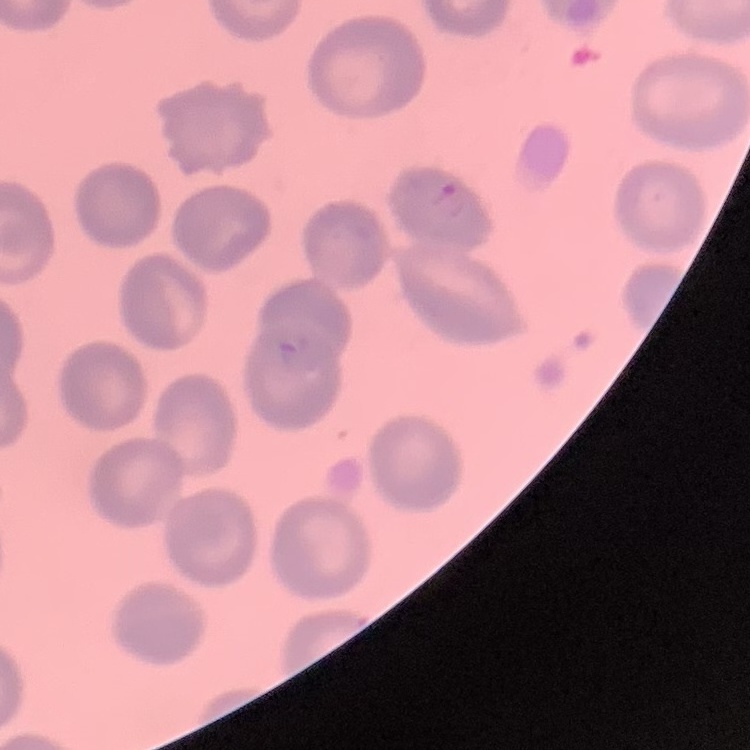
Summary:
  - Erythrocyte morphology: no rouleaux formation
  - Preparation: thin peripheral smear
  - Stain: Field's or Giemsa
  - Image type: one tile cut from a larger photomicrograph